Comment on the morphology of the red blood cells.
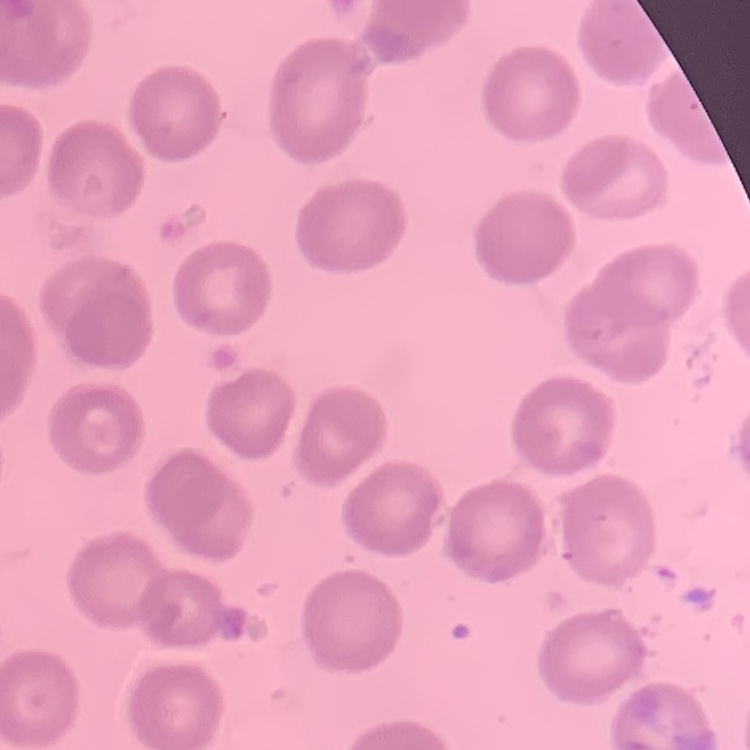

No rouleaux formation.

stain = Field's or Giemsa
preparation = thin blood smear
image type = square crop of a larger photomicrograph